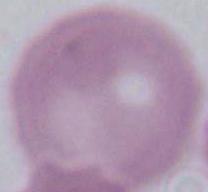
Summary:
  - Identification: red blood cell
  - Modality: micrograph
  - Magnification: 1000x